Locate every leukocyte (white blood cell).
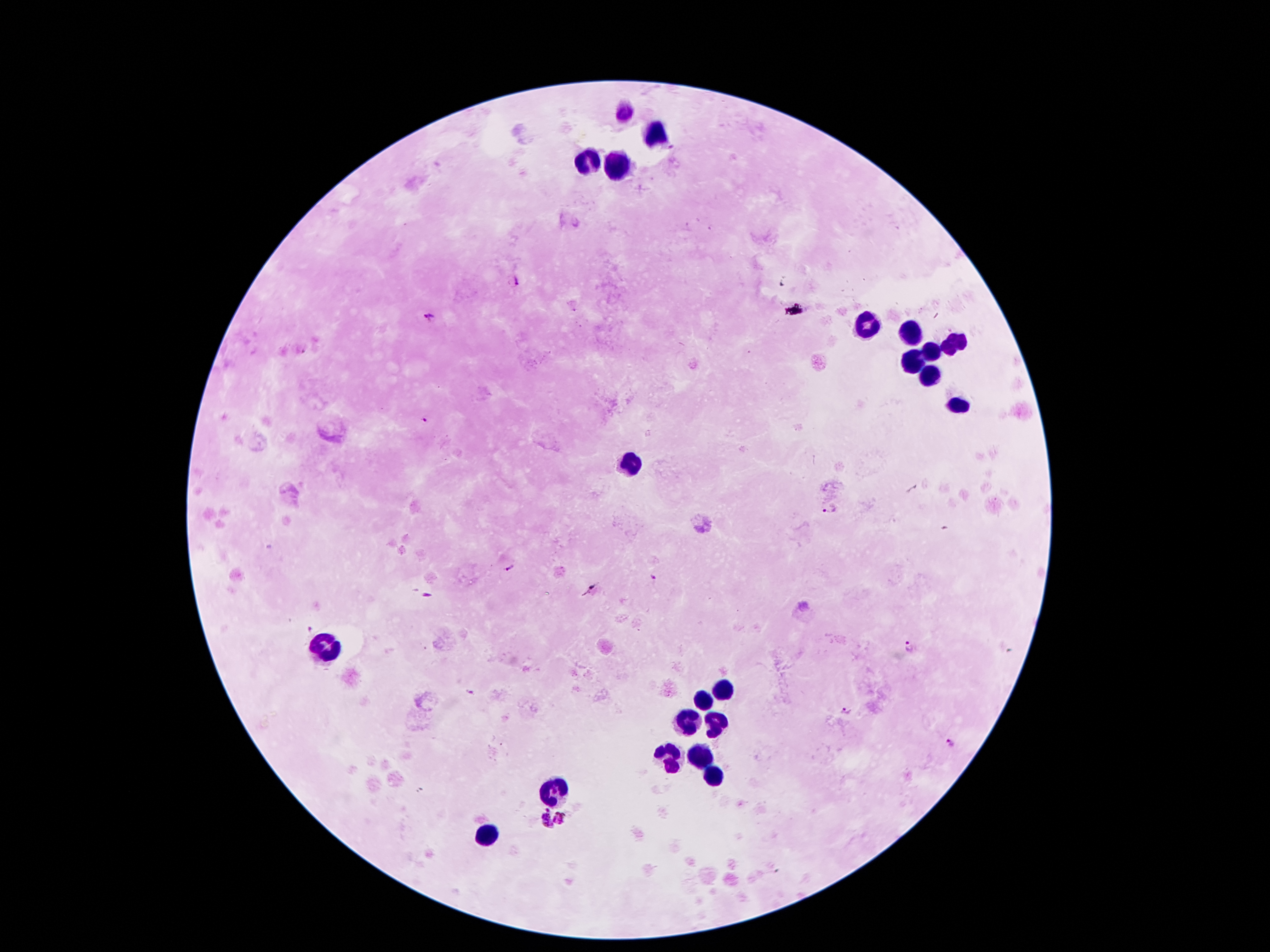

Approximate centers as [x, y] in pixels.
Leukocytes: [624, 112], [623, 114], [654, 141], [592, 163], [618, 168], [870, 327], [910, 334], [954, 343], [933, 354], [913, 363], [929, 377], [958, 405], [633, 461], [323, 650], [724, 693], [702, 704], [690, 725], [715, 725], [668, 759], [699, 759], [709, 772], [554, 789], [488, 831].

Plasmodium parasite locations: [514, 282], [431, 317], [425, 418], [829, 510], [508, 568], [651, 579], [426, 594], [307, 628], [909, 647], [469, 692], [845, 710], [948, 741], [562, 816], [542, 821]. Single field of view. Thick blood film. Patient malaria status: infected with Plasmodium falciparum. 100x magnification. Image is 1270×952 pixels. Photographed through the microscope eyepiece with a smartphone camera. Giemsa stain.